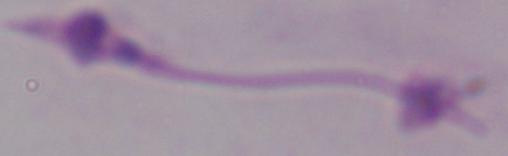
Captured at 1000x magnification. A Leishmania parasite is seen. Photomicrograph.